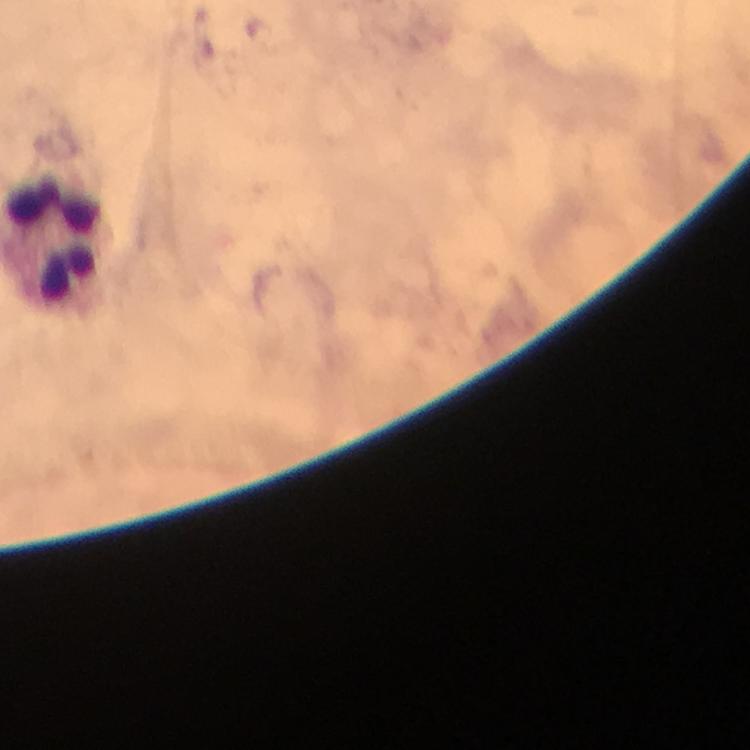 Approximate centers as (x, y) in pixels. Leukocyte locations: (55, 238). Immersion oil was used. From a malaria diagnostic workup. A crop from one field of view. Giemsa stain. Smartphone photograph taken through a microscope. 100x magnification. Image is 750×750 pixels. Plasmodium parasites: none detected. Thick blood film.